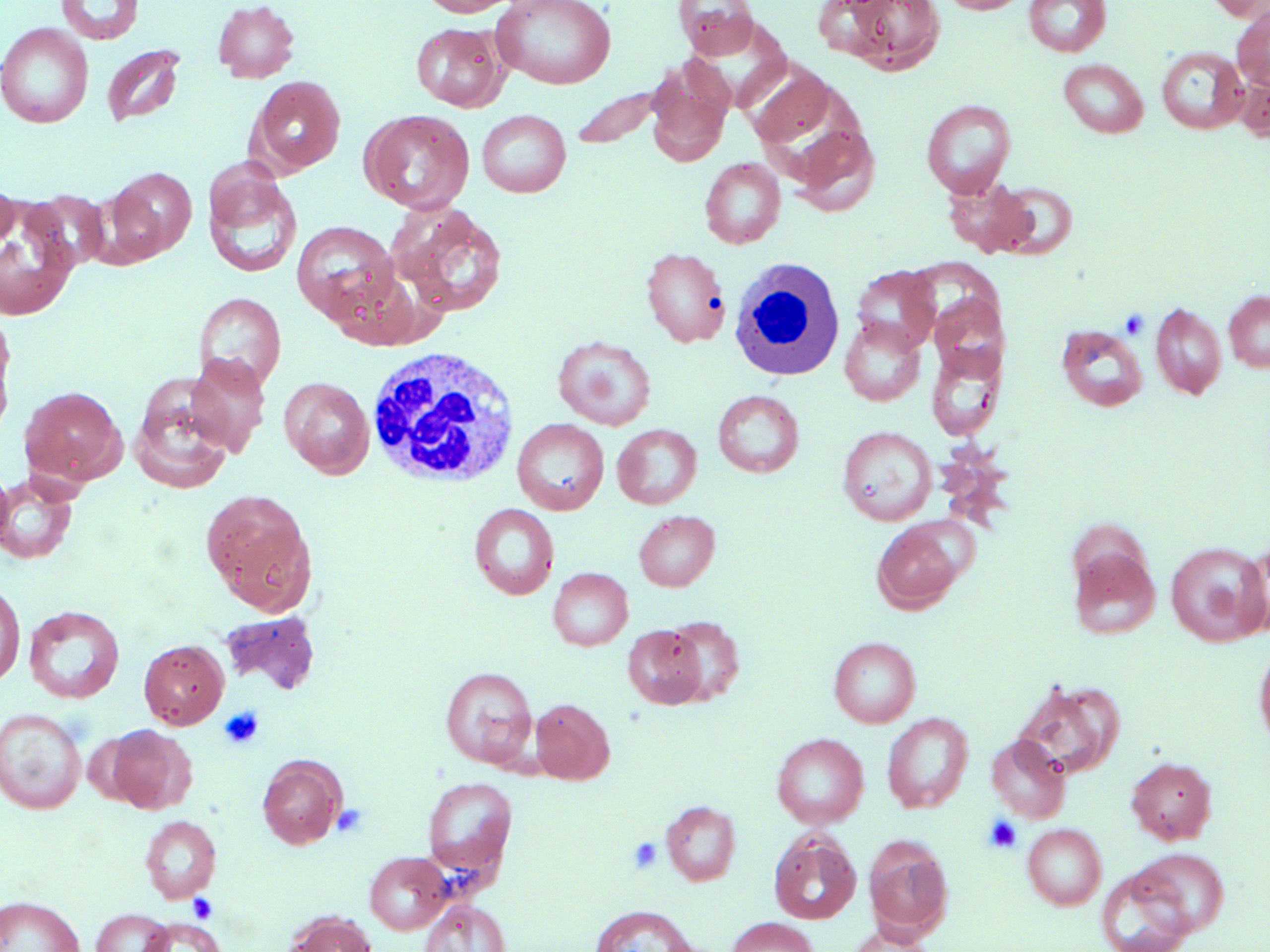

Approximate bounding boxes as named x1/y1/x2/y2 corners in pixels. White blood cell locations: (x1=728, y1=258, x2=845, y2=383), (x1=366, y1=347, x2=521, y2=488). Uninfected red blood cell locations: (x1=56, y1=0, x2=144, y2=44), (x1=212, y1=0, x2=300, y2=82), (x1=419, y1=0, x2=522, y2=17), (x1=673, y1=0, x2=761, y2=59), (x1=842, y1=0, x2=946, y2=74), (x1=938, y1=0, x2=1030, y2=14), (x1=1023, y1=0, x2=1112, y2=57), (x1=1205, y1=0, x2=1268, y2=20), (x1=491, y1=1, x2=616, y2=89), (x1=1232, y1=7, x2=1270, y2=91), (x1=0, y1=23, x2=94, y2=128), (x1=410, y1=23, x2=507, y2=111), (x1=101, y1=43, x2=186, y2=127), (x1=1156, y1=46, x2=1248, y2=135), (x1=1058, y1=58, x2=1148, y2=138), (x1=646, y1=62, x2=733, y2=166), (x1=744, y1=63, x2=837, y2=149), (x1=1234, y1=69, x2=1270, y2=141), (x1=247, y1=76, x2=346, y2=176), (x1=570, y1=85, x2=665, y2=150), (x1=921, y1=99, x2=1016, y2=198), (x1=360, y1=110, x2=475, y2=214), (x1=477, y1=110, x2=571, y2=198), (x1=790, y1=123, x2=881, y2=216), (x1=700, y1=157, x2=786, y2=248), (x1=203, y1=163, x2=302, y2=280), (x1=106, y1=167, x2=197, y2=262), (x1=943, y1=177, x2=1037, y2=258), (x1=992, y1=179, x2=1079, y2=258), (x1=0, y1=183, x2=18, y2=251), (x1=23, y1=190, x2=110, y2=271), (x1=389, y1=203, x2=509, y2=317), (x1=0, y1=209, x2=77, y2=320), (x1=292, y1=220, x2=399, y2=323), (x1=641, y1=247, x2=731, y2=347), (x1=851, y1=265, x2=940, y2=354), (x1=1224, y1=291, x2=1270, y2=372), (x1=193, y1=292, x2=286, y2=391), (x1=928, y1=293, x2=1007, y2=380), (x1=1150, y1=301, x2=1227, y2=399), (x1=0, y1=313, x2=17, y2=436), (x1=840, y1=316, x2=926, y2=406), (x1=1055, y1=324, x2=1148, y2=412), (x1=553, y1=335, x2=657, y2=431), (x1=926, y1=342, x2=1006, y2=441), (x1=184, y1=352, x2=271, y2=456), (x1=129, y1=377, x2=235, y2=494), (x1=280, y1=377, x2=375, y2=478), (x1=21, y1=386, x2=127, y2=485), (x1=712, y1=389, x2=804, y2=477), (x1=512, y1=419, x2=609, y2=515), (x1=612, y1=423, x2=702, y2=509), (x1=838, y1=425, x2=936, y2=525), (x1=0, y1=461, x2=13, y2=554), (x1=0, y1=472, x2=79, y2=565), (x1=201, y1=489, x2=317, y2=613), (x1=469, y1=503, x2=559, y2=600), (x1=634, y1=510, x2=720, y2=591), (x1=871, y1=520, x2=966, y2=613), (x1=1237, y1=540, x2=1270, y2=641), (x1=1166, y1=541, x2=1269, y2=646), (x1=1069, y1=546, x2=1161, y2=640), (x1=548, y1=567, x2=633, y2=650), (x1=0, y1=581, x2=25, y2=687), (x1=23, y1=605, x2=125, y2=703), (x1=221, y1=611, x2=320, y2=694), (x1=662, y1=615, x2=745, y2=705), (x1=623, y1=625, x2=706, y2=708), (x1=828, y1=637, x2=921, y2=727), (x1=139, y1=639, x2=229, y2=728), (x1=1253, y1=642, x2=1270, y2=755), (x1=440, y1=666, x2=537, y2=767), (x1=1015, y1=679, x2=1124, y2=780), (x1=530, y1=698, x2=614, y2=783), (x1=0, y1=707, x2=86, y2=813), (x1=882, y1=712, x2=974, y2=813), (x1=104, y1=724, x2=196, y2=813), (x1=771, y1=733, x2=869, y2=828), (x1=986, y1=734, x2=1071, y2=823), (x1=257, y1=755, x2=345, y2=848), (x1=1126, y1=756, x2=1217, y2=844), (x1=422, y1=776, x2=517, y2=878), (x1=661, y1=800, x2=741, y2=886), (x1=139, y1=815, x2=221, y2=902), (x1=1022, y1=823, x2=1107, y2=910), (x1=769, y1=831, x2=861, y2=924), (x1=864, y1=836, x2=953, y2=940), (x1=1130, y1=847, x2=1230, y2=938), (x1=365, y1=851, x2=451, y2=934), (x1=1096, y1=866, x2=1195, y2=952), (x1=0, y1=895, x2=83, y2=952), (x1=420, y1=899, x2=510, y2=952), (x1=589, y1=904, x2=696, y2=952), (x1=90, y1=908, x2=173, y2=952), (x1=283, y1=911, x2=378, y2=952), (x1=726, y1=916, x2=820, y2=952), (x1=139, y1=918, x2=225, y2=952), (x1=845, y1=924, x2=939, y2=952). Platelet locations: (x1=1119, y1=308, x2=1149, y2=340), (x1=219, y1=706, x2=265, y2=750), (x1=331, y1=804, x2=369, y2=838), (x1=984, y1=816, x2=1022, y2=853), (x1=628, y1=837, x2=663, y2=873), (x1=188, y1=893, x2=218, y2=923). Slide-level diagnosis: no evidence of blood parasites. Image is 1270×952 pixels. One field of a larger specimen. Light microscopy. Thin blood smear. May-Grünwald-Giemsa-stained preparation. Captured at 1000x magnification.